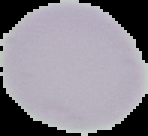
From a thin blood film. Image is 148×136 pixels. Malaria status: uninfected. Cell region segmented out of the field of view; the surrounding area is masked to black.